Name the blood parasite species.
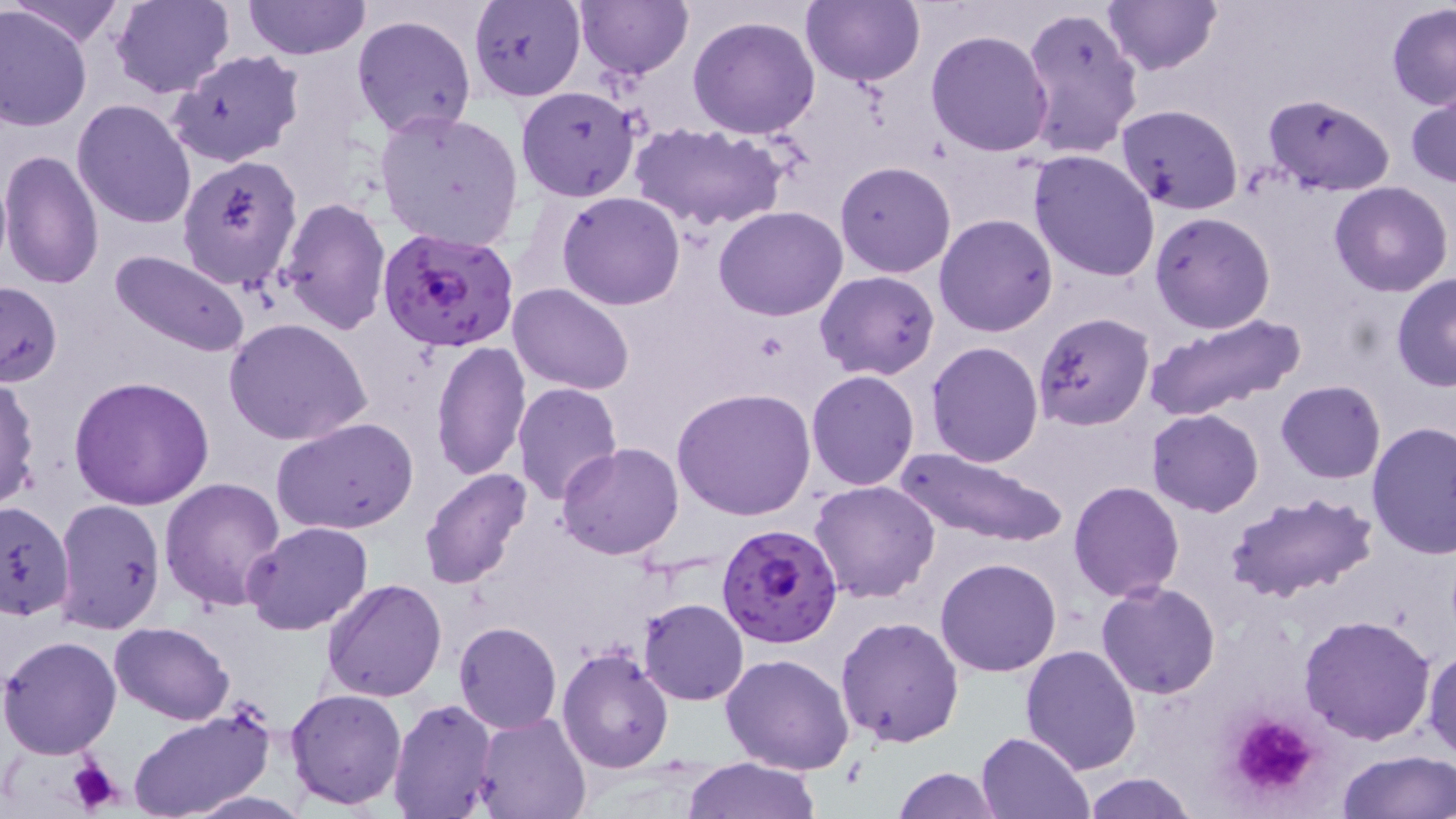
Plasmodium falciparum.

Approximate bounding boxes as (x1,y1)-(x2,y2) corner pairs in pixels. Plasmodium falciparum-infected red blood cell locations: (377,228)-(520,354), (717,522)-(844,647). Platelet locations: (1225,711)-(1319,800), (63,759)-(125,816). Uninfected red blood cell locations: (10,0)-(125,47), (109,0)-(235,99), (242,0)-(367,60), (574,0)-(691,77), (802,0)-(925,87), (1101,0)-(1221,76), (469,1)-(586,102), (1386,2)-(1456,111), (1019,4)-(1144,162), (0,6)-(94,131), (351,13)-(477,140), (688,15)-(820,139), (926,30)-(1055,156), (167,51)-(305,167), (516,84)-(642,203), (1407,84)-(1456,190), (1263,92)-(1395,198), (73,100)-(197,230), (1117,103)-(1244,213), (375,109)-(525,251), (630,122)-(788,233), (0,148)-(105,290), (1028,149)-(1162,281), (176,155)-(303,289), (835,161)-(956,279), (1330,182)-(1453,297), (558,191)-(685,310), (278,197)-(392,336), (714,206)-(849,321), (1149,211)-(1276,334), (934,213)-(1057,336), (108,249)-(253,359), (816,270)-(940,381), (1390,273)-(1456,392), (0,281)-(63,388), (509,284)-(634,395), (1143,311)-(1306,420), (1032,312)-(1155,432), (224,318)-(373,445), (431,340)-(531,483), (927,340)-(1044,467), (806,370)-(921,491), (0,373)-(40,512), (69,374)-(215,511), (1276,379)-(1385,483), (511,381)-(623,504), (671,387)-(816,521), (1146,408)-(1263,515), (270,417)-(420,535), (1366,422)-(1456,559), (556,442)-(685,560), (894,445)-(1067,551), (418,468)-(534,592), (160,477)-(288,612), (809,480)-(941,604), (1068,480)-(1184,602), (1225,491)-(1377,606), (54,497)-(165,634), (0,500)-(75,621), (243,521)-(373,636), (935,557)-(1062,678), (322,578)-(448,702), (1097,581)-(1222,699), (639,598)-(748,704), (1299,613)-(1437,745), (836,615)-(965,747), (108,622)-(235,726), (452,622)-(561,733), (0,635)-(123,758), (1020,644)-(1142,775), (1423,644)-(1456,762), (555,646)-(674,774), (721,653)-(856,775), (285,688)-(408,809), (388,697)-(498,817), (127,706)-(276,819), (475,712)-(592,819), (977,731)-(1093,818), (1335,748)-(1456,819), (683,757)-(821,818), (893,767)-(1002,819), (1082,773)-(1200,819). One field of a larger specimen. May-Grünwald-Giemsa-stained preparation. Thin blood film. Captured at 1000x magnification. Optical microscopy. Image is 1456×819 pixels.